Comment on the morphology of the erythrocytes.
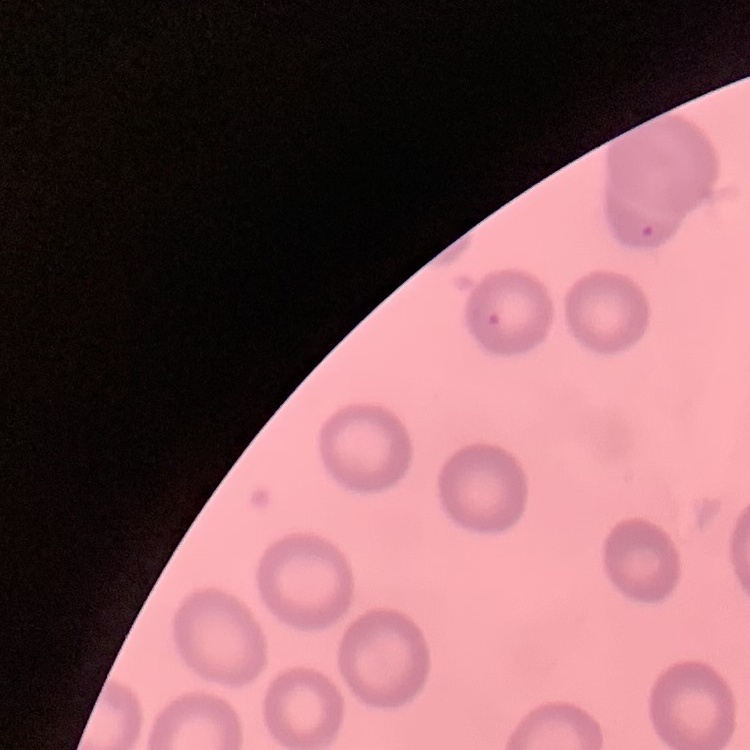

They show no rouleaux formation.

{
  "stain": "Field's or Giemsa",
  "preparation": "thin blood smear",
  "image_type": "one tile cut from a larger photomicrograph"
}